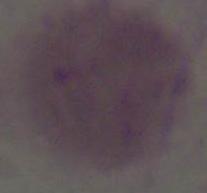
Summary:
  - Magnification: 1000x
  - Modality: micrograph
  - Identification: red blood cell